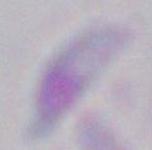
Photomicrograph. Toxoplasma gondii is shown. Captured at 1000x magnification.